Name the parasite shown.
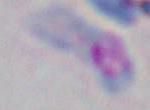

This is Toxoplasma gondii.

Micrograph. 1000x magnification.